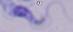

Summary:
  - Magnification: 1000x
  - Identification: trypanosome
  - Modality: micrograph